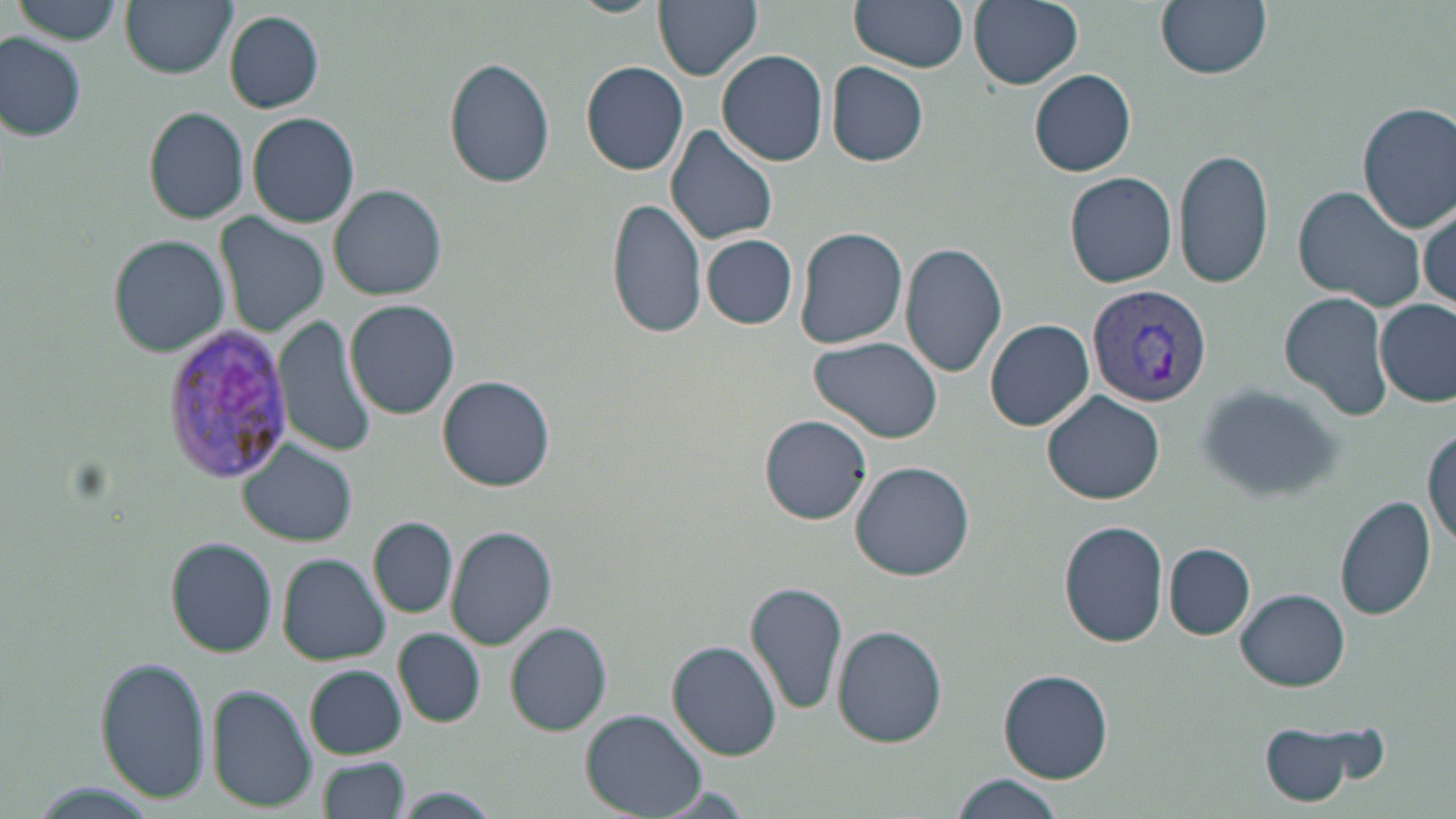 Approximate bounding boxes as (x1, y1, x2, y2) in pixels. Uninfected red blood cell locations: (119, 0, 235, 78), (564, 0, 663, 17), (654, 0, 763, 79), (849, 0, 968, 73), (969, 0, 1083, 89), (1155, 0, 1272, 79), (13, 1, 124, 46), (224, 10, 324, 113), (0, 34, 87, 142), (717, 49, 829, 166), (444, 57, 555, 189), (581, 61, 689, 175), (827, 61, 930, 166), (1029, 69, 1137, 177), (1357, 102, 1456, 231), (143, 107, 249, 224), (247, 112, 360, 228), (665, 123, 779, 246), (1173, 145, 1274, 293), (1065, 172, 1177, 287), (330, 183, 447, 300), (1292, 184, 1426, 313), (607, 195, 707, 342), (1417, 199, 1454, 315), (214, 213, 330, 337), (793, 225, 907, 350), (109, 235, 229, 356), (702, 235, 797, 329), (899, 241, 1008, 378), (1281, 293, 1390, 419), (1374, 299, 1454, 405), (346, 300, 461, 420), (275, 315, 377, 457), (986, 319, 1095, 431), (809, 336, 945, 444), (438, 376, 552, 491), (1192, 383, 1349, 505), (1042, 392, 1167, 506), (759, 415, 872, 525), (1425, 426, 1455, 552), (237, 442, 356, 547), (850, 460, 974, 579), (1335, 495, 1437, 622), (370, 516, 457, 618), (1059, 521, 1170, 647), (446, 523, 558, 650), (164, 537, 279, 657), (1165, 544, 1255, 639), (280, 554, 390, 665), (745, 579, 849, 717), (1236, 589, 1350, 690), (506, 621, 611, 736), (833, 625, 947, 749), (394, 628, 484, 727), (668, 641, 781, 760), (95, 655, 211, 805), (306, 665, 406, 758), (999, 669, 1113, 784), (207, 686, 315, 810), (583, 710, 705, 817), (1253, 715, 1384, 808), (317, 757, 409, 819), (947, 776, 1068, 818), (21, 783, 164, 817), (395, 787, 495, 819). Plasmodium vivax-infected red blood cell locations: (1086, 283, 1213, 407), (164, 324, 292, 482). Slide-level diagnosis: Plasmodium vivax. 1000x magnification. May-Grünwald-Giemsa stain. Light microscopy. Image is 1456×819 pixels. Single field of view. Thin blood film.